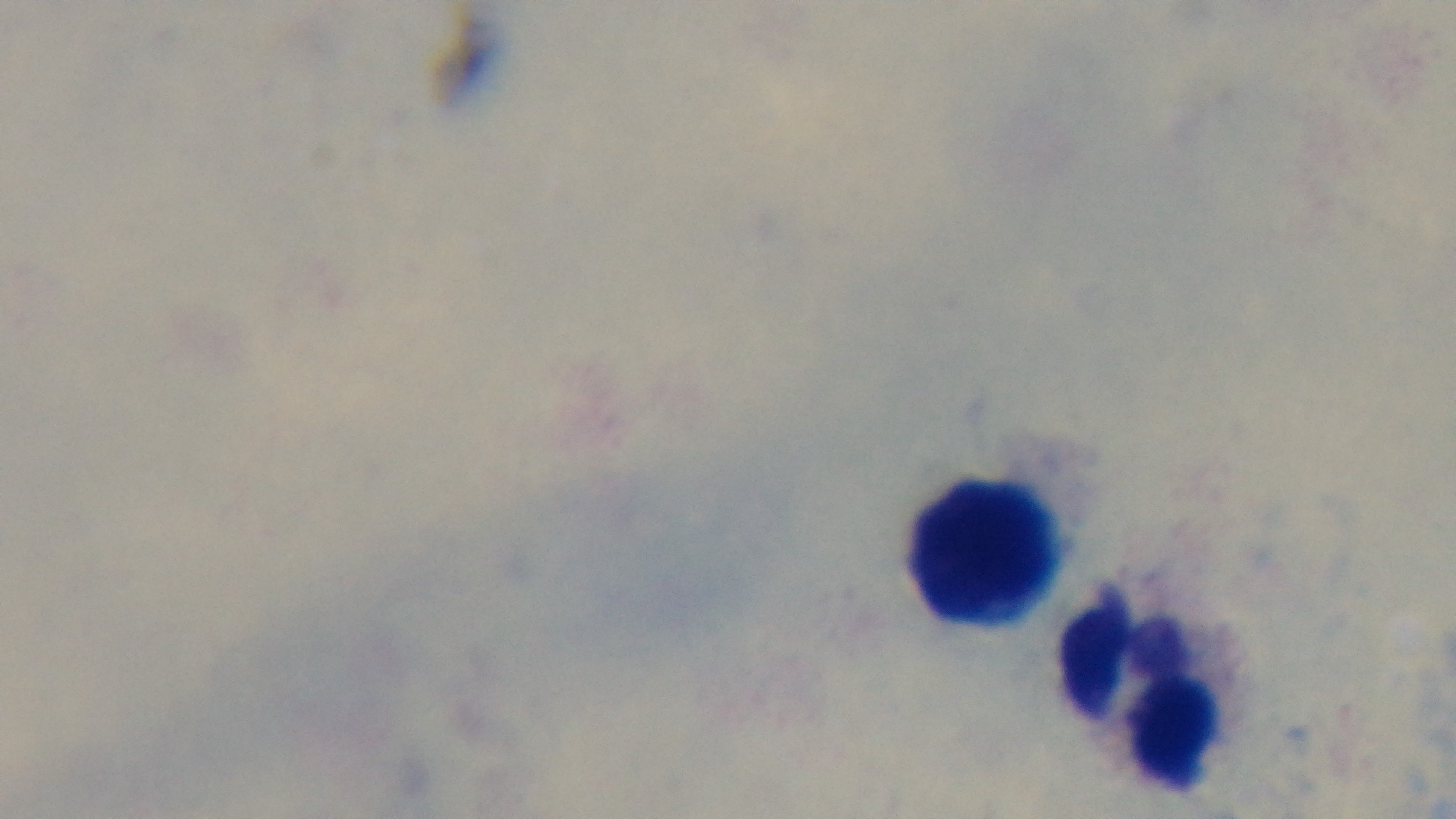

Summary:
  - Capture: mounted 4K digital camera
  - Objective: 100x oil immersion
  - Modality: light microscopy
  - Stain: Giemsa
  - Preparation: thick blood film
  - Field of view: one from the slide
  - Malaria status: negative